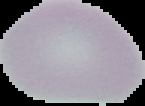

Image is 145×106 pixels. The area outside the segmented cell region is set to black. From a thin blood smear. Malaria status: uninfected.